Outline each blood parasite and name the species.
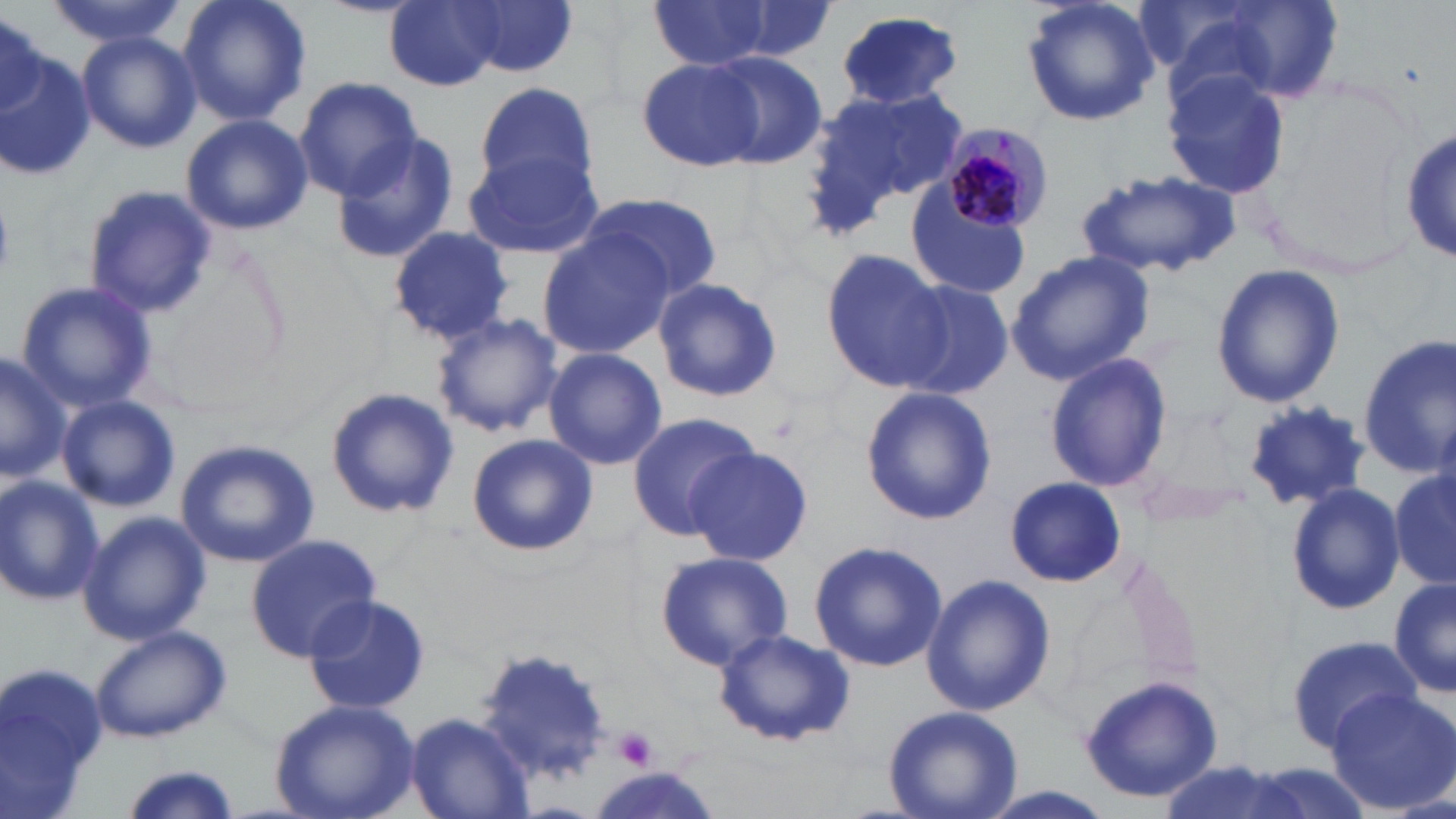

Approximate bounding boxes as (x1, y1, x2, y2) in pixels.
Plasmodium malariae-infected red blood cells: (941, 120, 1054, 232).
No Plasmodium falciparum, Plasmodium ovale, Plasmodium vivax, Babesia divergens, or Trypanosoma brucei observed.

Uninfected red blood cell locations: (45, 0, 191, 46), (178, 0, 311, 128), (385, 0, 505, 91), (1019, 0, 1161, 128), (1162, 0, 1339, 110), (459, 1, 578, 77), (648, 1, 774, 72), (0, 7, 45, 114), (834, 9, 964, 111), (76, 32, 199, 152), (0, 49, 98, 182), (703, 51, 827, 169), (635, 57, 772, 173), (1162, 68, 1288, 199), (294, 76, 422, 201), (476, 81, 599, 194), (806, 86, 970, 225), (180, 113, 313, 235), (1403, 124, 1456, 268), (331, 132, 459, 266), (465, 149, 606, 262), (1078, 170, 1242, 279), (905, 176, 1033, 302), (84, 185, 218, 318), (581, 191, 723, 301), (540, 225, 671, 360), (386, 226, 515, 346), (821, 248, 953, 394), (1004, 251, 1157, 385), (1210, 265, 1346, 409), (652, 278, 783, 403), (14, 279, 157, 413), (897, 279, 1014, 400), (431, 312, 562, 437), (1356, 335, 1456, 480), (543, 348, 667, 470), (0, 350, 69, 486), (1045, 352, 1171, 493), (325, 387, 459, 519), (861, 387, 995, 526), (58, 395, 181, 512), (1244, 402, 1371, 510), (626, 410, 760, 539), (466, 433, 596, 558), (174, 439, 321, 569), (685, 447, 812, 566), (1390, 467, 1454, 595), (1132, 469, 1257, 530), (0, 474, 105, 606), (1004, 477, 1125, 585), (1280, 485, 1405, 617), (77, 508, 210, 646), (245, 534, 381, 660), (809, 539, 948, 672), (654, 550, 796, 672), (920, 572, 1056, 716), (1389, 575, 1455, 699), (301, 594, 432, 715), (90, 625, 230, 744), (713, 628, 855, 747), (1284, 634, 1417, 745), (469, 646, 614, 788), (0, 658, 106, 816), (1078, 677, 1225, 802), (1324, 685, 1456, 814), (268, 699, 420, 819), (882, 706, 1024, 819), (405, 713, 529, 816), (1154, 761, 1307, 819), (119, 763, 243, 819). Platelet locations: (614, 726, 657, 771). Slide-level diagnosis: Plasmodium malariae. Image is 1456×819 pixels. Optical microscopy. May-Grünwald-Giemsa-stained preparation. 1000x magnification. Single field of view. Thin blood film.